Classify this cell by malaria status.
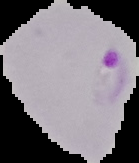
It is parasitized.

Summary:
  - Preparation: thin blood film
  - Image size: 139×163 pixels
  - Image type: cell region segmented out of the field of view; surrounding area masked to black